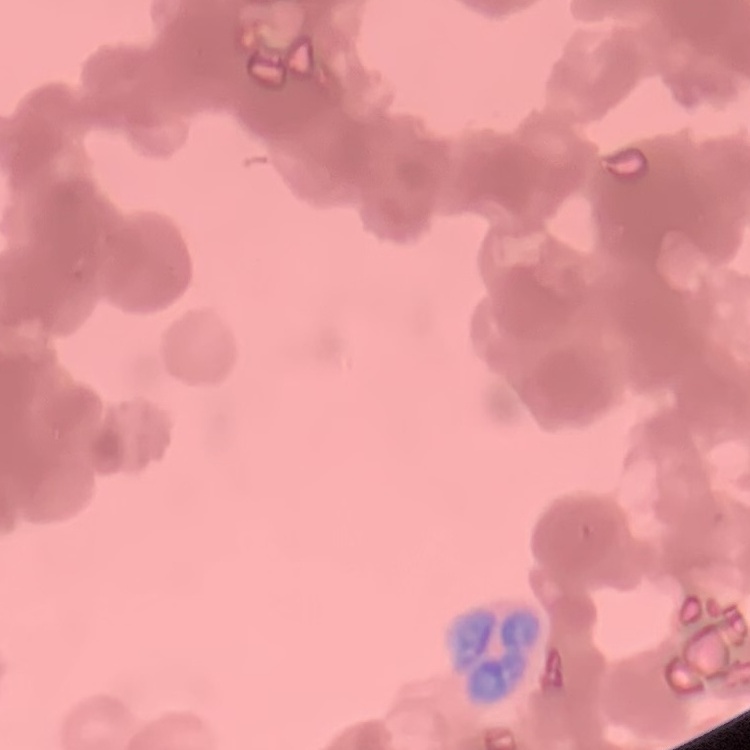

Summary:
  - Red blood cell morphology: rouleaux formation
  - Image type: square crop of a larger photomicrograph
  - Stain: Field's or Giemsa
  - Preparation: thin peripheral smear